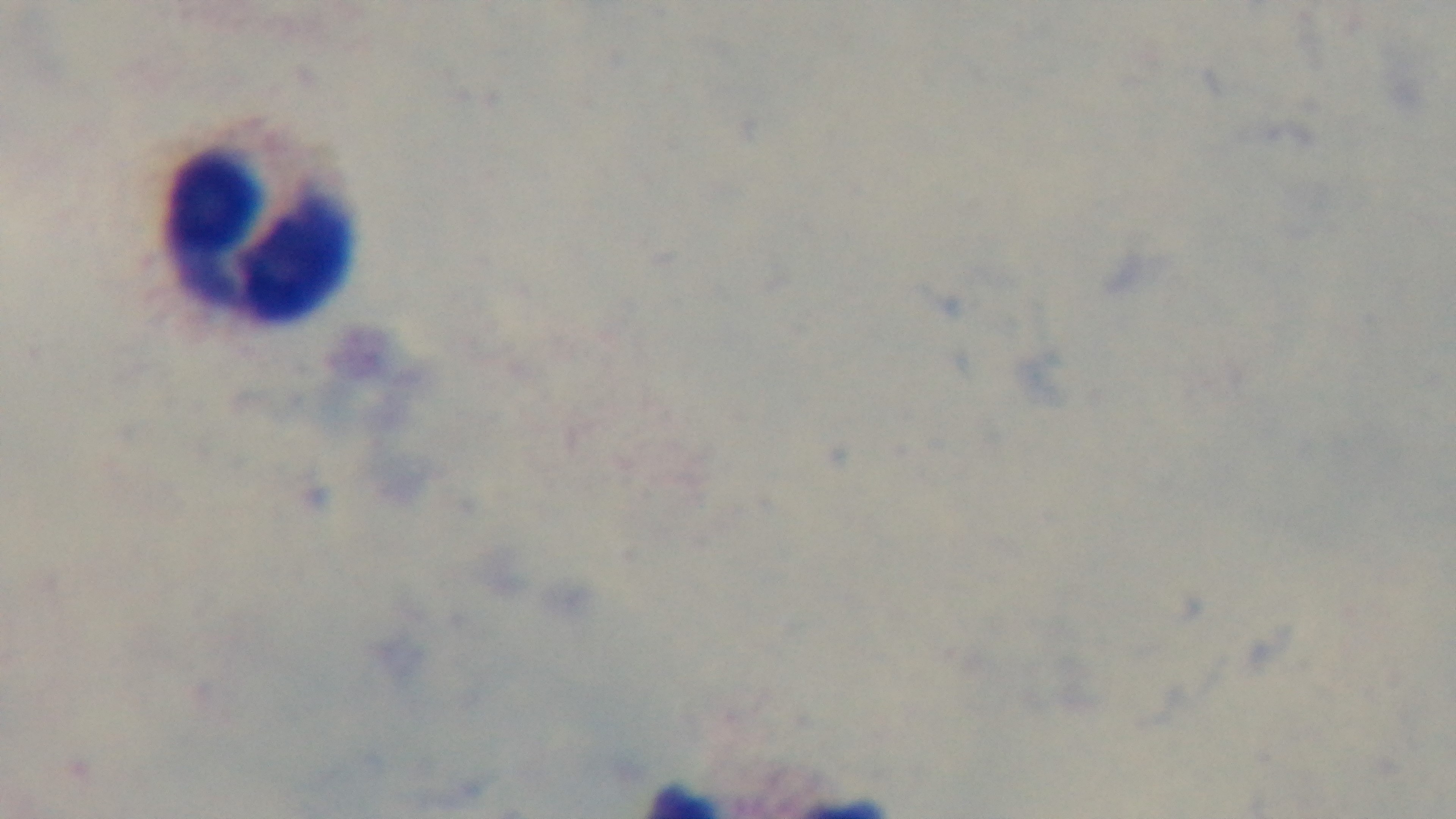 Single field of view. Mounted 4K digital camera. Malaria status: negative. Light microscopy. Giemsa stain. Oil-immersion objective, 100x. Preparation: thick smear.